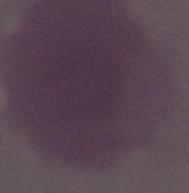

Photomicrograph. 1000x magnification. A red blood cell is seen.